Identify the cell.
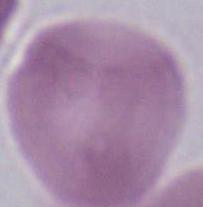

An erythrocyte.

modality = photomicrograph
magnification = 1000x